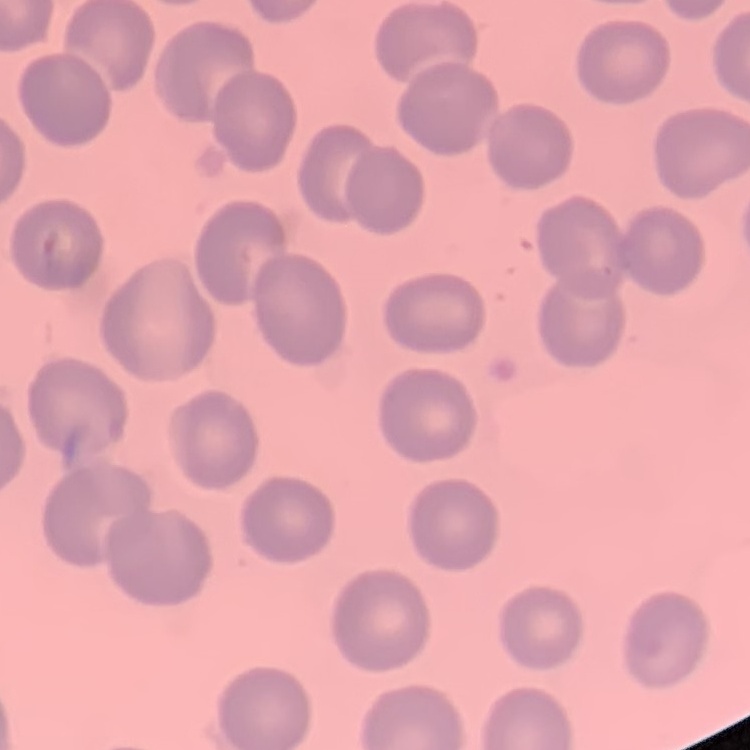

erythrocyte_morphology: no rouleaux formation
stain: Field's or Giemsa
preparation: thin blood smear
image_type: square crop of a larger photomicrograph